Assess this cell for malaria.
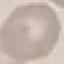

Uninfected.

stain = Giemsa
preparation = thin blood smear
capture = smartphone camera at the microscope eyepiece
image type = automatically extracted cell patch, resized to 64 × 64 pixels